Assess this cell for malaria.
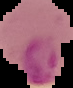
Parasitized.

From a thin blood smear. Image is 73×88 pixels. Segmented cell region on a black background.